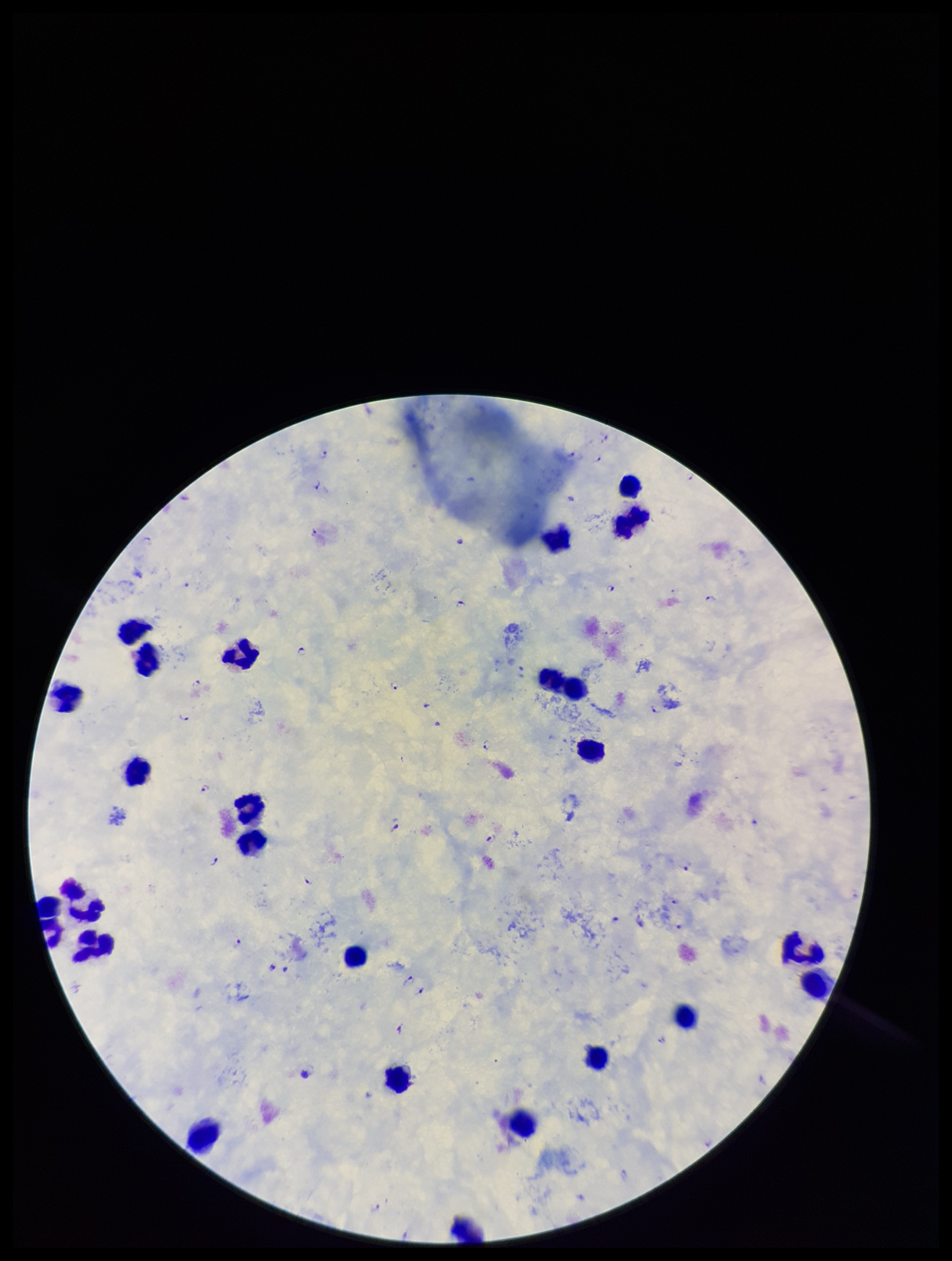
Summary:
  - Leukocyte count: 26
  - Capture: smartphone photograph through the microscope eyepiece
  - Field of view: one from this slide
  - Species reported for this patient: Plasmodium falciparum
  - Parasite count: 30
  - Plasmodium parasites: seen
  - Image size: 952×1261 pixels
  - Patient malaria status: positive
  - Stain: Giemsa
  - Preparation: thick blood smear